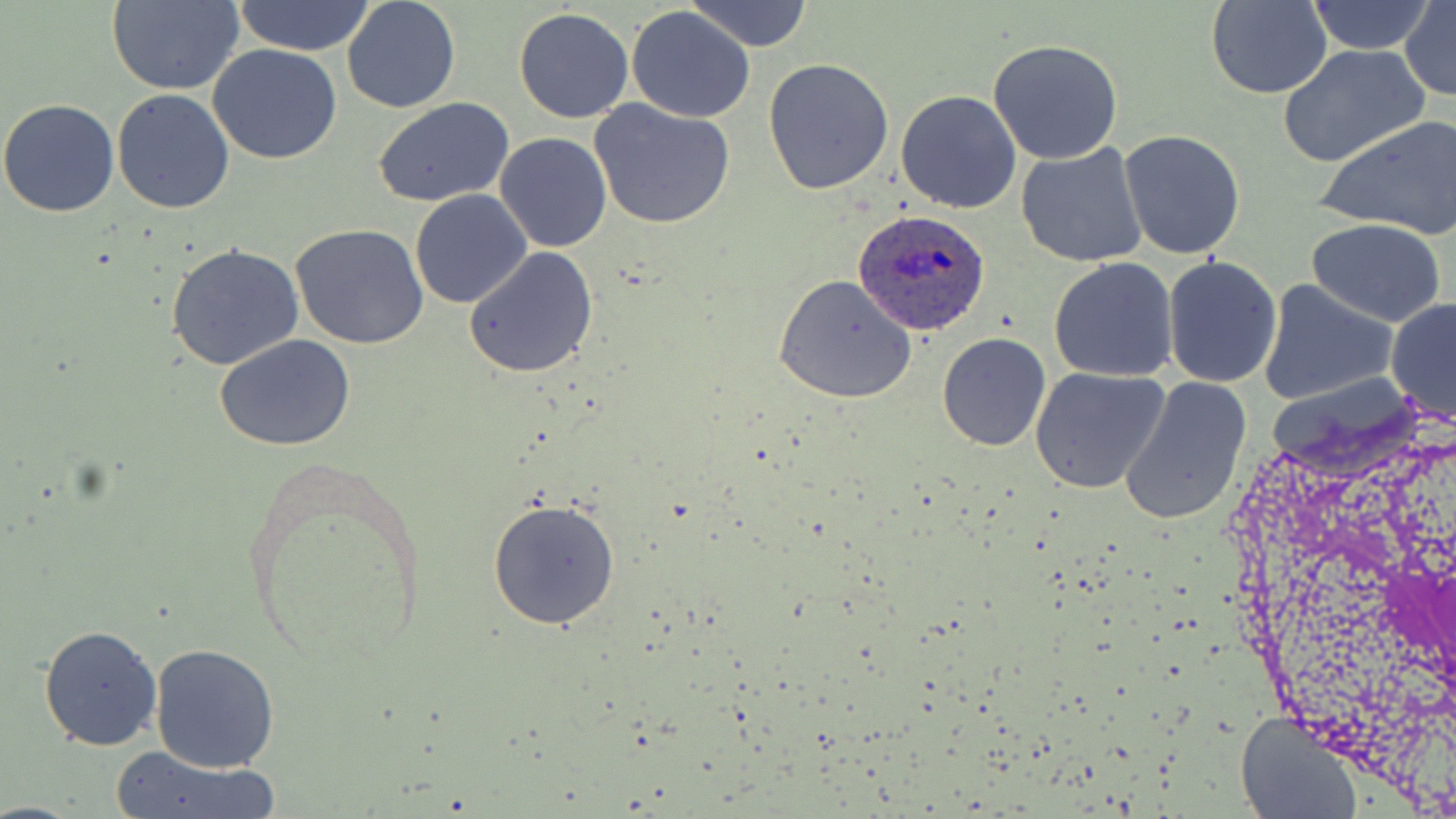

Approximate bounding boxes as [x1, y1, x2, y2] in pixels. Plasmodium ovale-infected red blood cell locations: [853, 210, 990, 336]. Uninfected red blood cell locations: [233, 0, 377, 56], [342, 0, 460, 114], [684, 0, 814, 50], [1304, 0, 1438, 54], [106, 1, 243, 95], [1205, 1, 1332, 99], [1400, 2, 1455, 101], [626, 5, 756, 123], [514, 8, 635, 124], [987, 38, 1124, 165], [209, 43, 343, 165], [1276, 45, 1428, 168], [763, 57, 896, 195], [112, 88, 235, 213], [894, 89, 1022, 213], [373, 97, 518, 204], [589, 98, 736, 230], [0, 99, 120, 218], [1317, 114, 1456, 239], [1118, 129, 1248, 261], [495, 133, 613, 253], [1015, 142, 1149, 267], [409, 188, 534, 309], [1306, 218, 1447, 327], [290, 224, 429, 350], [166, 242, 306, 372], [464, 246, 600, 379], [1162, 256, 1284, 390], [1048, 257, 1179, 383], [772, 274, 917, 404], [1259, 278, 1398, 407], [1385, 296, 1456, 425], [936, 331, 1052, 452], [214, 334, 358, 454], [1030, 367, 1171, 497], [1120, 376, 1252, 526], [487, 497, 622, 631], [40, 625, 163, 750], [149, 643, 280, 774], [1235, 712, 1361, 819], [106, 745, 279, 819]. Slide-level diagnosis: Plasmodium ovale. Light microscopy. One field of a larger specimen. May-Grünwald-Giemsa stain. 1000x magnification. Thin blood film. Image is 1456×819 pixels.